Classify this cell by malaria status.
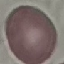

It is uninfected.

{
  "image_type": "cell patch, automatically extracted from a larger field of view and resized to 64 × 64 pixels",
  "stain": "Giemsa",
  "preparation": "thin blood film",
  "capture": "smartphone camera at the microscope eyepiece"
}